Give the preparation type.
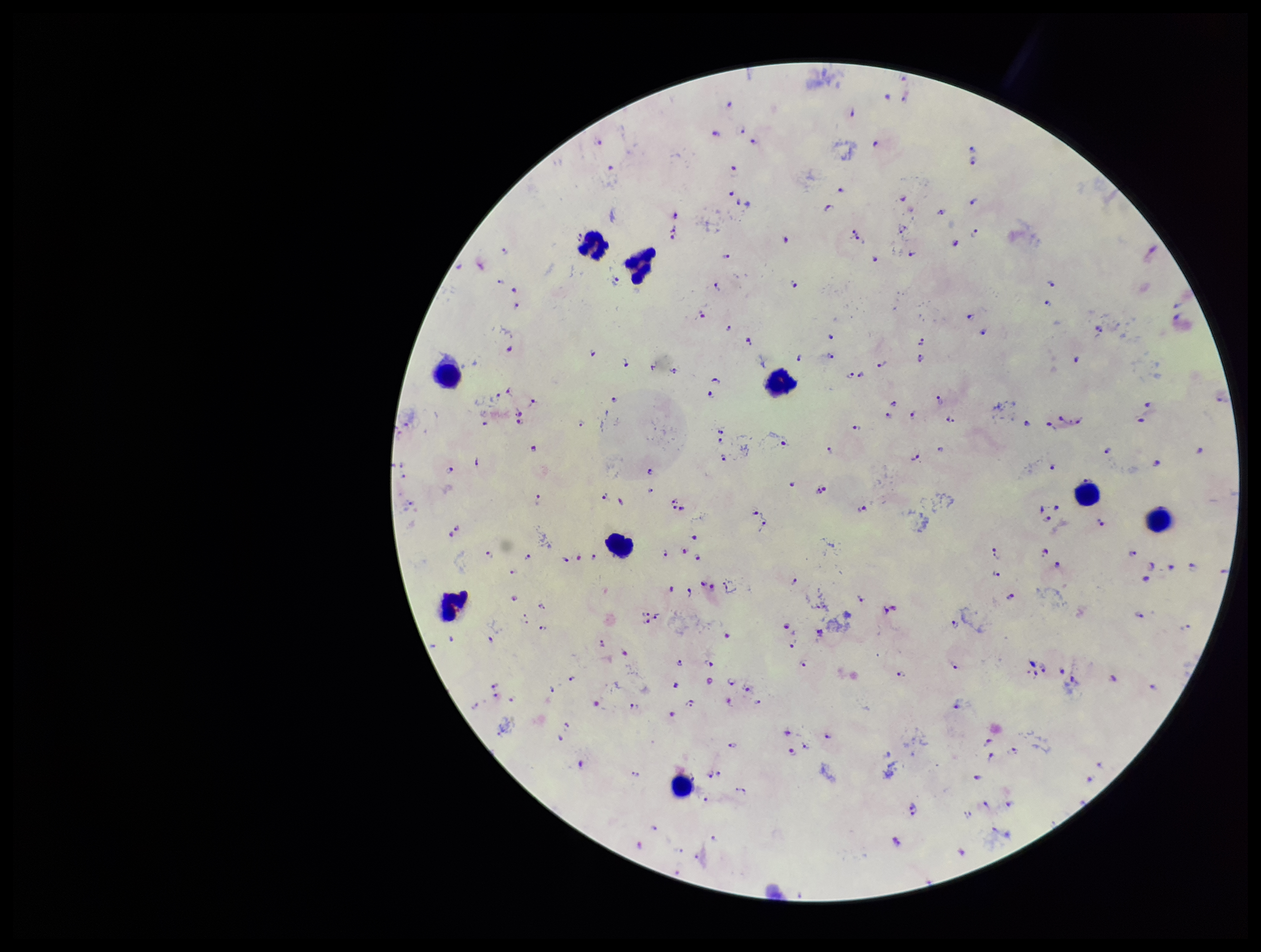
Thick.

One field from this slide. Species reported for this patient: Plasmodium falciparum. Leukocyte count: 9. Parasite count: 170. Patient malaria status: positive. Plasmodium parasites: identified. Image is 1261×952 pixels. Smartphone photograph taken through the eyepiece of a microscope. Giemsa stain.